Outline each blood parasite and name the species.
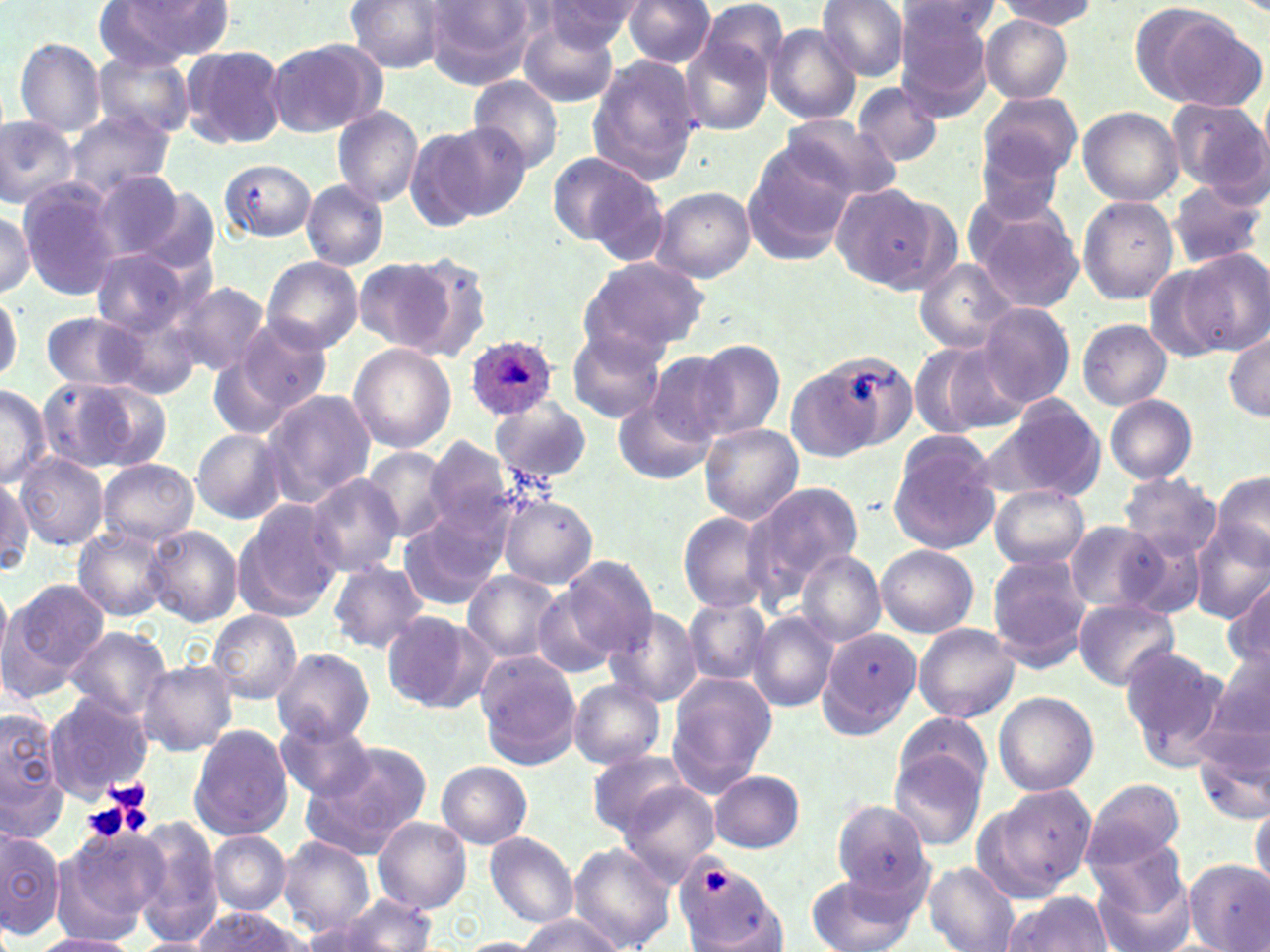
Approximate bounding boxes as (x1,y1)-(x2,y2) corner pairs in pixels.
Plasmodium ovale-infected red blood cells: (464,334)-(556,420).
No Plasmodium falciparum, Plasmodium malariae, Plasmodium vivax, Babesia divergens, or Trypanosoma brucei observed.

slide_level_diagnosis: Plasmodium ovale
preparation: thin blood smear
uninfected_red_blood_cell_locations: 'approximate bounding boxes as (x1,y1)-(x2,y2) corner pairs in pixels: (344,0)-(450,72), (541,0)-(645,50), (622,0)-(716,69), (695,0)-(791,92), (815,0)-(912,81), (995,0)-(1096,28), (97,1)-(231,68), (422,1)-(540,87), (1131,2)-(1265,112), (894,3)-(999,51), (895,4)-(995,120), (517,11)-(620,107), (981,16)-(1072,103), (765,24)-(862,124), (678,29)-(775,137), (265,38)-(385,139), (14,39)-(106,135), (181,44)-(287,148), (91,52)-(196,139), (586,56)-(703,185), (467,75)-(564,173), (851,80)-(944,167), (977,91)-(1081,186), (1168,97)-(1267,197), (331,104)-(423,209), (1078,108)-(1183,205), (777,113)-(900,206), (0,114)-(79,209), (64,114)-(175,199), (407,122)-(521,228), (975,139)-(1068,223), (740,143)-(859,263), (546,151)-(660,252), (217,159)-(317,242), (90,169)-(186,263), (17,180)-(122,300), (1166,180)-(1265,269), (302,181)-(388,270), (829,184)-(951,292), (133,187)-(219,273), (654,187)-(757,282), (964,191)-(1083,308), (1077,195)-(1178,303), (0,207)-(35,300), (1181,248)-(1270,355), (90,251)-(196,336), (397,252)-(495,362), (262,256)-(363,353), (353,256)-(460,355), (577,256)-(710,358), (915,260)-(1020,354), (170,280)-(272,377), (0,291)-(22,384), (103,302)-(205,397), (978,303)-(1074,406), (40,312)-(154,393), (230,317)-(332,421), (1077,319)-(1172,409), (1225,328)-(1270,421), (567,329)-(665,422), (908,341)-(1024,437), (695,342)-(785,440), (348,343)-(457,455), (785,346)-(903,462), (643,350)-(737,447), (207,351)-(296,442), (38,376)-(169,474), (0,384)-(51,487), (260,388)-(374,506), (1104,393)-(1197,483), (988,395)-(1106,503), (491,397)-(593,486), (614,397)-(714,485), (700,424)-(803,524), (191,430)-(286,524), (889,431)-(999,554), (423,440)-(515,539), (359,448)-(453,543), (14,454)-(108,549), (98,459)-(198,547), (1211,469)-(1270,570), (1119,473)-(1222,559), (305,475)-(405,578), (0,478)-(32,576), (251,481)-(386,596), (741,481)-(864,600), (989,485)-(1087,570), (498,494)-(598,588), (230,500)-(345,622), (676,510)-(777,615), (400,511)-(508,610), (1063,519)-(1172,615), (1190,523)-(1270,625), (145,525)-(241,626), (73,527)-(172,621), (1117,532)-(1211,619), (876,545)-(978,638), (796,551)-(886,646), (987,555)-(1090,668), (558,557)-(658,661), (327,561)-(429,652), (464,570)-(561,663), (3,576)-(113,693), (0,580)-(12,676), (1223,582)-(1269,671), (537,583)-(622,677), (683,597)-(771,686), (1074,599)-(1178,690), (604,606)-(704,705), (209,610)-(301,705), (380,611)-(488,713), (749,612)-(840,713), (913,623)-(1021,723), (62,626)-(171,722), (818,626)-(922,739), (1210,642)-(1270,748), (1121,643)-(1232,767), (270,648)-(375,744), (477,655)-(579,768), (138,661)-(237,756), (666,673)-(779,793), (568,681)-(666,768), (993,691)-(1099,796), (43,694)-(152,801), (1,709)-(67,829), (896,711)-(993,801), (275,721)-(379,801), (188,724)-(293,842), (1193,735)-(1270,826), (305,744)-(430,856), (890,749)-(987,851), (588,750)-(693,836), (438,761)-(532,848), (710,770)-(804,852), (1084,777)-(1186,868), (618,782)-(721,884), (976,784)-(1096,901), (834,799)-(931,896), (1250,801)-(1269,895), (129,815)-(223,941), (373,817)-(471,912), (57,825)-(165,935), (0,826)-(63,938), (209,831)-(290,912), (485,832)-(578,927), (277,836)-(376,935), (570,843)-(674,950), (1088,845)-(1196,952), (1185,861)-(1270,952), (674,862)-(782,949), (925,864)-(1020,952), (808,874)-(919,952), (1002,891)-(1117,951), (334,893)-(436,951), (189,907)-(312,951), (297,912)-(395,951), (513,914)-(622,952), (33,933)-(140,952), (455,936)-(543,951), (132,937)-(216,952)'
stain: May-Grünwald-Giemsa
field_of_view: single
image_size: 1270×952 pixels
magnification: 1000x
platelet_locations: 'approximate bounding boxes as (x1,y1)-(x2,y2) corner pairs in pixels: (101,776)-(155,827), (82,801)-(130,842), (697,868)-(728,897)'
modality: light microscopy